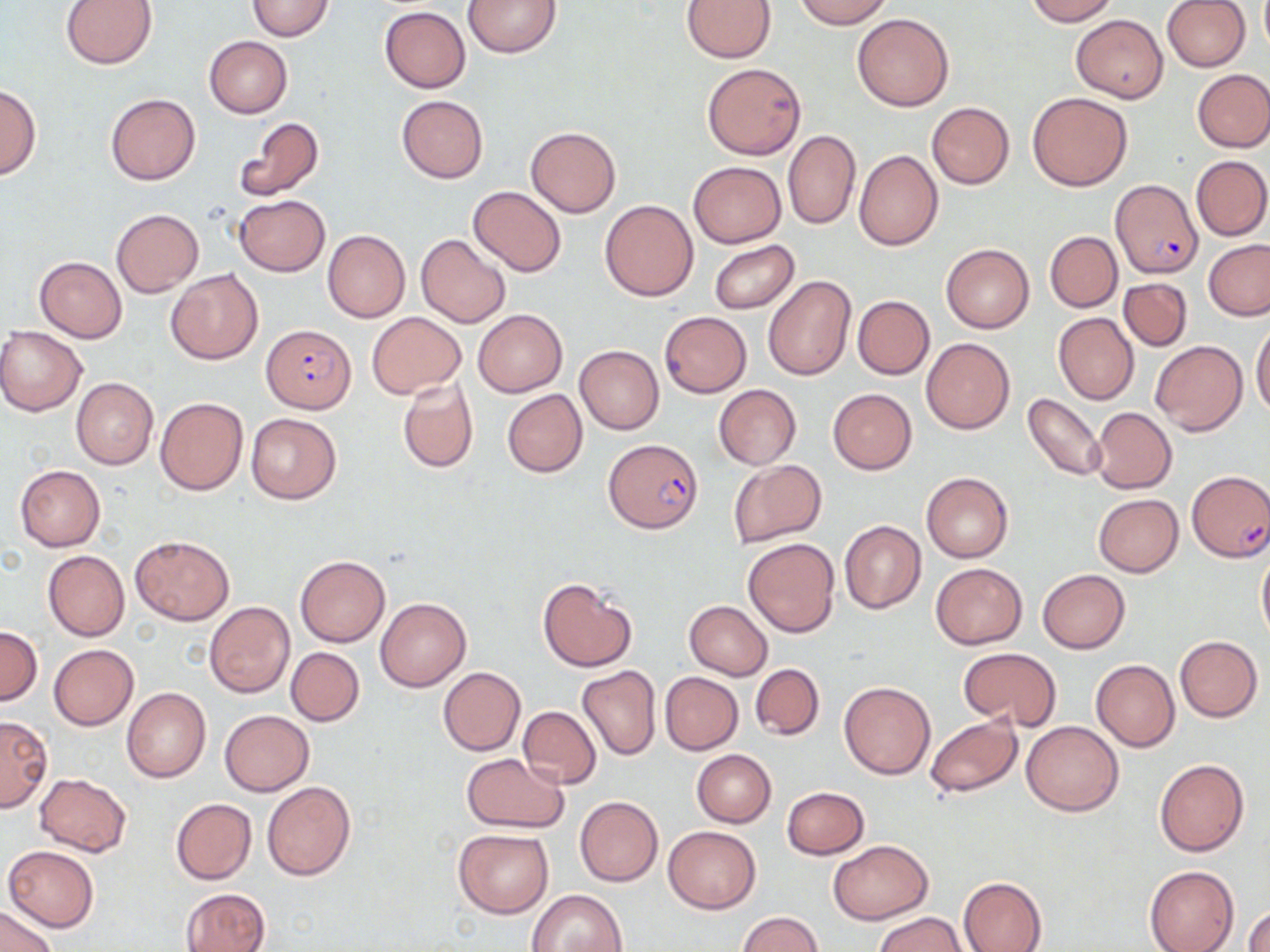
slide-level diagnosis = Plasmodium falciparum
field of view = one of a larger specimen
modality = light microscopy
Plasmodium falciparum-infected red blood cell locations = approximate bounding boxes as [x1, y1, x2, y2] in pixels: [1109, 179, 1203, 278], [261, 325, 357, 412], [604, 439, 702, 532], [1187, 471, 1269, 563]
preparation = thin blood smear
uninfected red blood cell locations = approximate bounding boxes as [x1, y1, x2, y2] in pixels: [61, 0, 158, 68], [464, 0, 561, 57], [682, 0, 777, 62], [793, 0, 893, 28], [1023, 0, 1119, 24], [246, 1, 334, 40], [1162, 1, 1251, 73], [379, 6, 470, 93], [852, 14, 953, 111], [1070, 14, 1168, 102], [204, 36, 293, 117], [702, 63, 806, 159], [1192, 69, 1270, 153], [0, 84, 41, 180], [1027, 91, 1132, 191], [106, 94, 201, 185], [397, 95, 488, 182], [926, 101, 1014, 189], [234, 117, 325, 202], [526, 126, 621, 216], [782, 129, 861, 229], [853, 149, 942, 250], [1191, 154, 1270, 241], [687, 161, 786, 247], [467, 185, 567, 277], [235, 194, 329, 276], [599, 200, 698, 301], [110, 208, 204, 297], [323, 230, 411, 322], [1045, 231, 1122, 311], [416, 234, 510, 328], [1203, 239, 1270, 321], [708, 241, 799, 314], [941, 243, 1034, 334], [35, 256, 127, 342], [166, 269, 264, 364], [763, 275, 857, 381], [1119, 278, 1191, 350], [1124, 279, 1207, 404], [853, 296, 934, 379], [472, 309, 567, 397], [367, 311, 466, 399], [659, 311, 751, 397], [1053, 312, 1139, 405], [1251, 324, 1270, 416], [0, 326, 86, 415], [922, 338, 1014, 434], [1150, 339, 1248, 435], [575, 345, 664, 434], [71, 377, 158, 470], [397, 377, 478, 474], [714, 385, 800, 468], [828, 388, 917, 474], [503, 389, 587, 477], [1023, 393, 1109, 482], [154, 397, 248, 496], [1090, 407, 1177, 494], [245, 413, 341, 504], [728, 461, 827, 548], [14, 465, 105, 550], [921, 472, 1014, 563], [1093, 494, 1184, 577], [839, 521, 926, 613], [130, 535, 234, 624], [742, 537, 839, 638], [1256, 546, 1270, 646], [42, 550, 129, 641], [295, 555, 390, 647], [930, 562, 1029, 649], [1037, 569, 1130, 653], [537, 576, 638, 673], [375, 596, 470, 691], [684, 600, 773, 680], [204, 601, 295, 698], [0, 626, 42, 706], [1174, 635, 1262, 722], [48, 644, 139, 730], [286, 646, 364, 726], [958, 647, 1062, 732], [1090, 659, 1180, 752], [751, 663, 825, 740], [577, 665, 661, 761], [437, 666, 525, 755], [660, 672, 742, 754], [838, 681, 936, 779], [121, 686, 211, 783], [518, 705, 601, 788], [220, 710, 313, 795], [0, 715, 51, 811], [924, 715, 1024, 799], [1021, 719, 1124, 815], [691, 749, 776, 826], [460, 752, 568, 833], [1154, 758, 1250, 857], [34, 773, 132, 857], [262, 780, 357, 881], [782, 786, 870, 859], [575, 796, 663, 886], [170, 798, 257, 884], [663, 825, 761, 913], [453, 829, 555, 918], [827, 839, 932, 925], [4, 845, 98, 930], [1144, 864, 1239, 952], [958, 877, 1048, 952], [180, 889, 268, 952], [527, 889, 628, 952], [1, 904, 58, 952], [1246, 907, 1270, 952], [738, 912, 823, 952], [876, 913, 967, 951]
stain = May-Grünwald-Giemsa
image size = 1270×952 pixels
magnification = 1000x